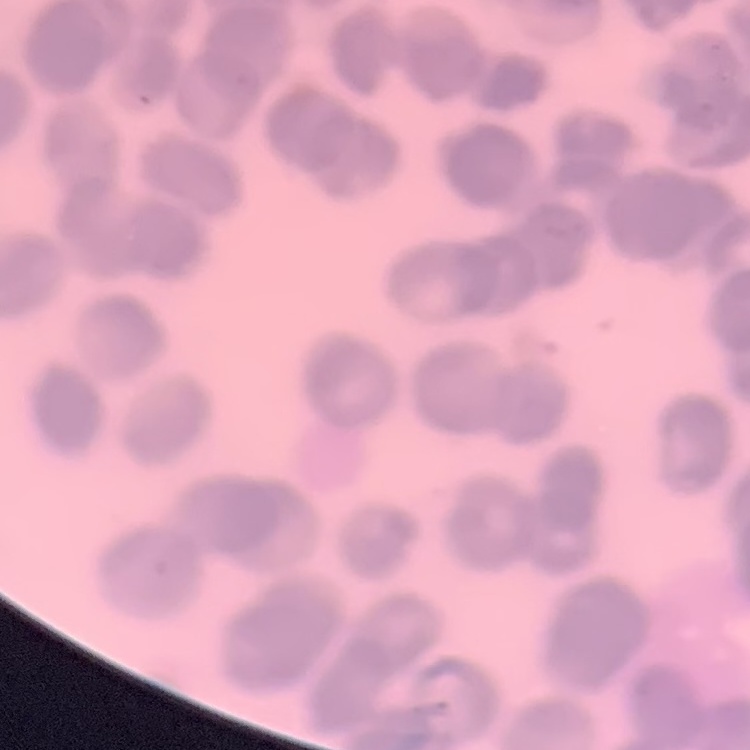
erythrocyte morphology = rouleaux formation
stain = Field's or Giemsa
preparation = thin blood smear
image type = one tile cut from a larger photomicrograph